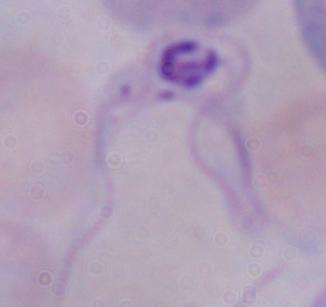 A trypanosome is shown. Captured at 1000x magnification. Photomicrograph.